Assess this cell for malaria.
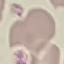

It is uninfected.

image type = cell patch, automatically extracted from a larger field of view and resized to 64 × 64 pixels
preparation = thin blood smear
stain = Giemsa
capture = smartphone camera at the microscope eyepiece